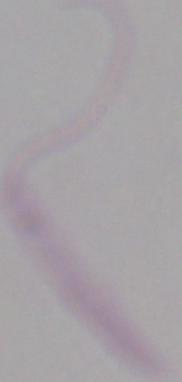
{
  "modality": "micrograph",
  "identification": "Leishmania",
  "magnification": "1000x"
}